Give the position of every Plasmodium parasite visible.
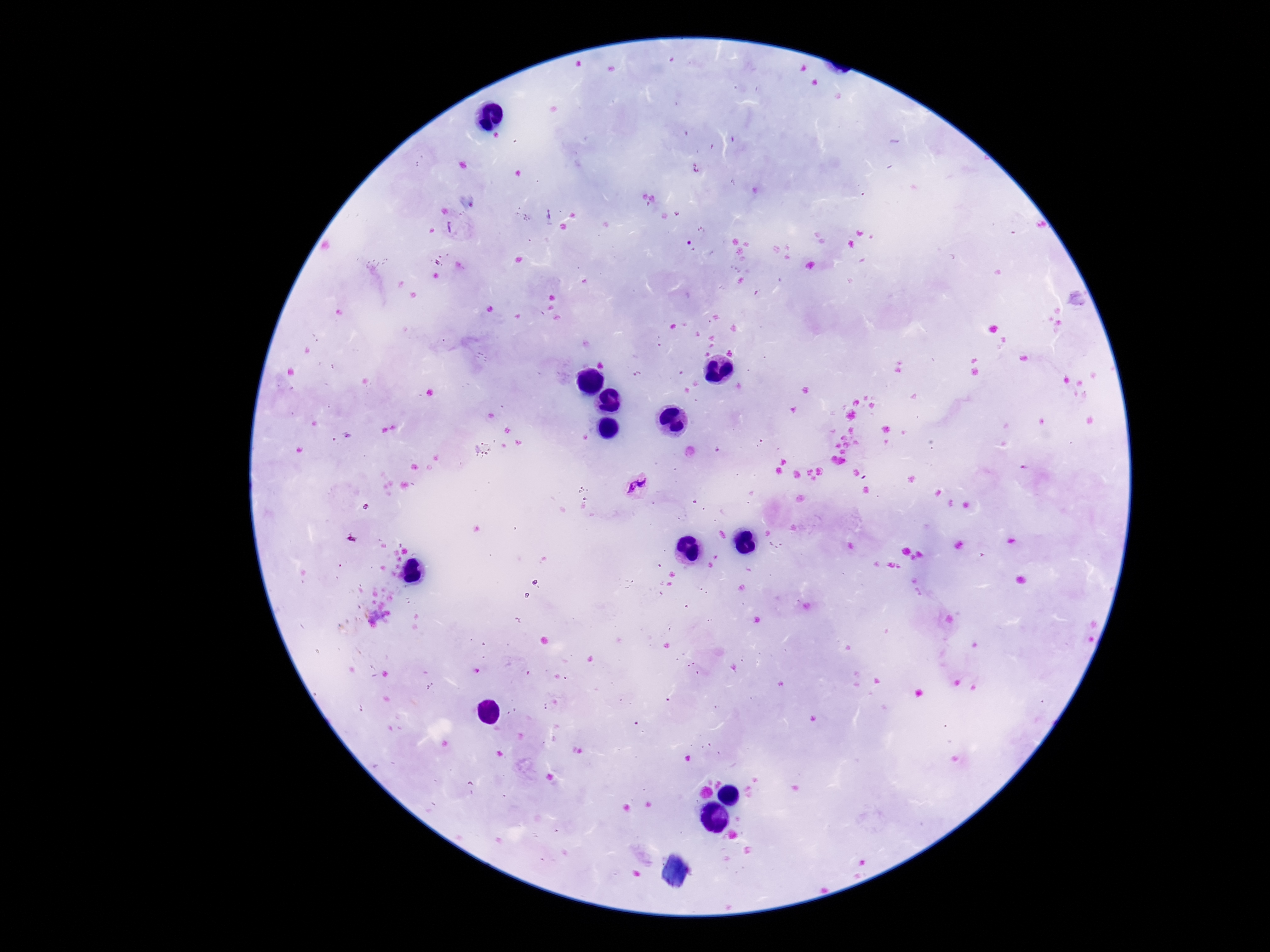

Approximate object centers, in pixels from the top-left corner.
Plasmodium parasites: (x=637, y=485).

Summary:
  - Preparation: thick peripheral-blood smear
  - Magnification: 100x
  - Patient malaria status: infected
  - Field of view: one from this slide
  - Image size: 1270×952 pixels
  - Capture: smartphone camera through the microscope eyepiece
  - Stain: Giemsa